Look for Plasmodium parasites.
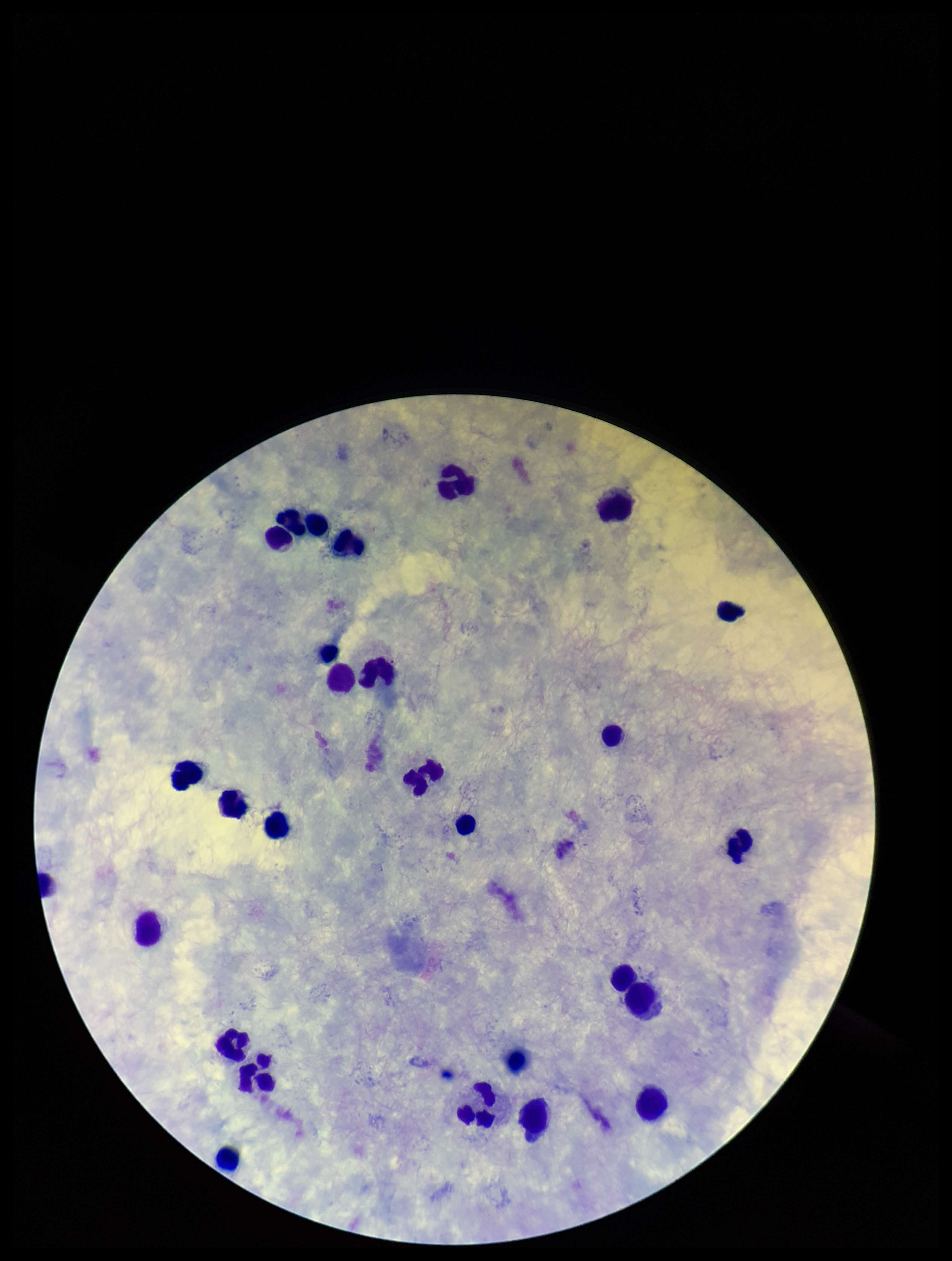
None identified.

Summary:
  - Leukocyte count: 27
  - Field of view: single
  - Preparation: thick
  - Capture: smartphone photograph through the microscope eyepiece
  - Parasite count: 0
  - Image size: 952×1261 pixels
  - Stain: Giemsa
  - Patient malaria status: negative